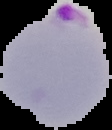

Summary:
  - Image type: cell region segmented out of the field of view; surrounding area masked to black
  - Image size: 112×130 pixels
  - Result: malaria parasites detected
  - Preparation: thin blood smear